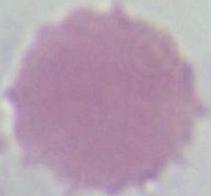
An erythrocyte is seen. Photomicrograph. 1000x magnification.